Comment on the morphology of the erythrocytes.
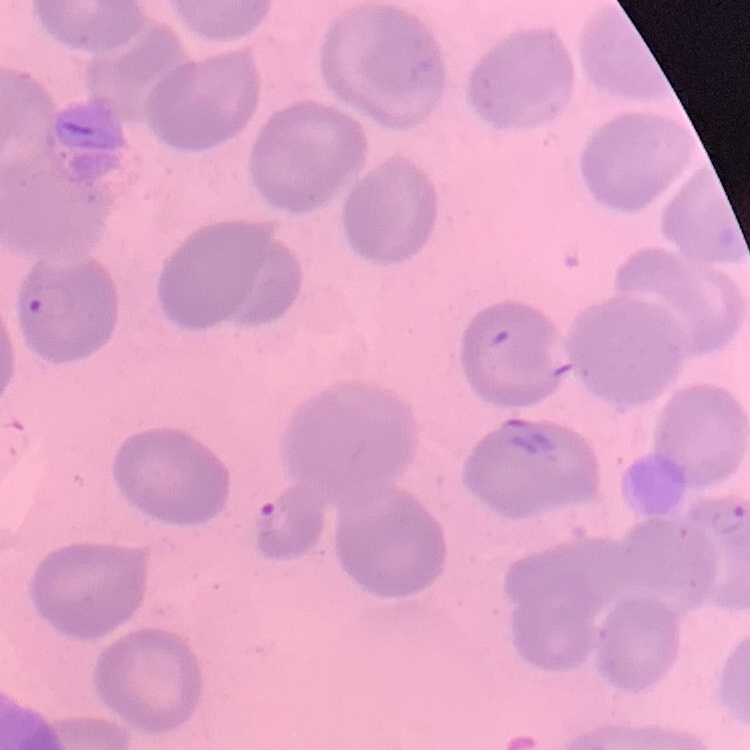

They show no rouleaux formation.

image_type: square crop of a larger photomicrograph
stain: Field's or Giemsa
preparation: thin blood film